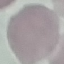
Summary:
  - Malaria status: uninfected
  - Image type: automatically extracted cell patch, resized to 64 × 64 pixels
  - Preparation: thin blood smear
  - Capture: smartphone through the microscope eyepiece
  - Stain: Giemsa